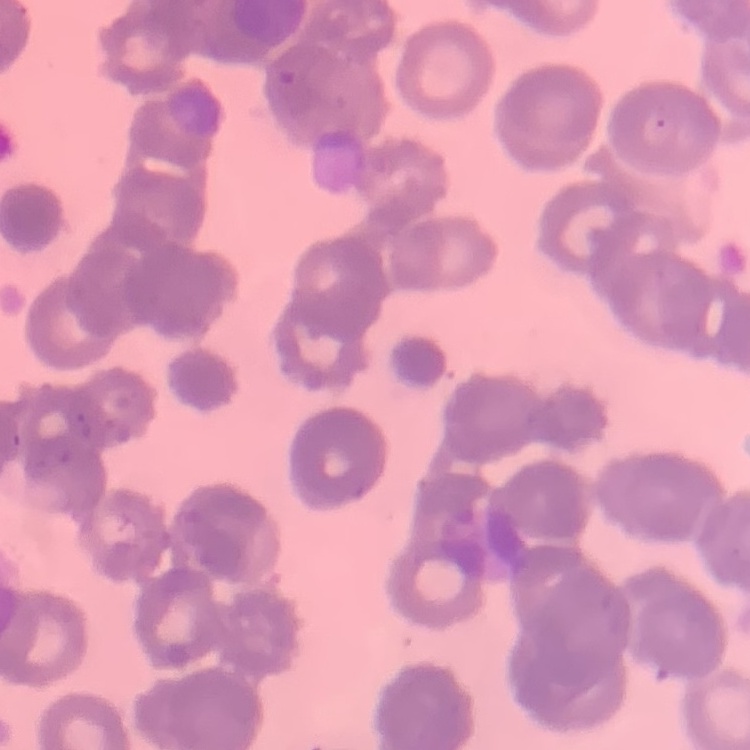

erythrocyte morphology = rouleaux formation
image type = square crop of a larger photomicrograph
preparation = thin blood smear
stain = Field's or Giemsa